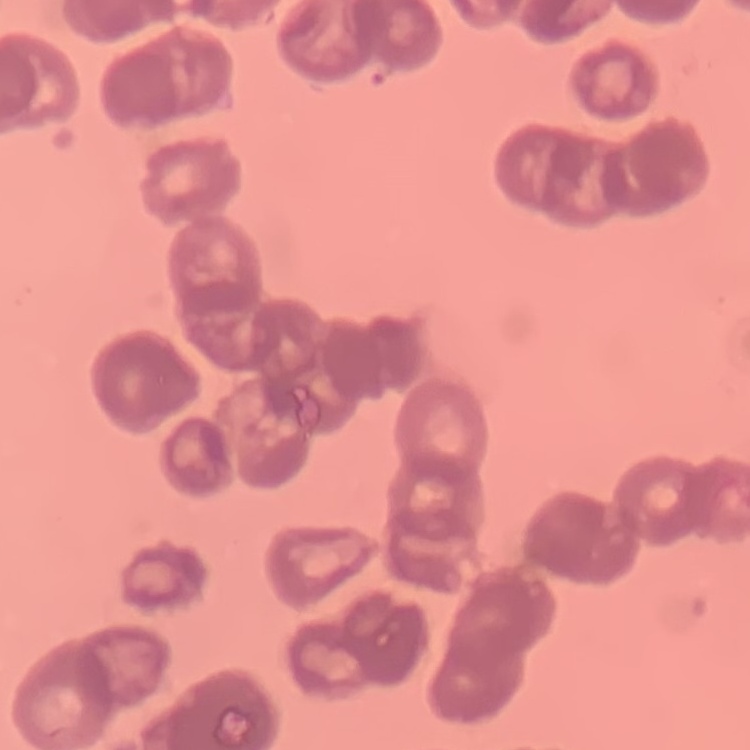
The erythrocytes show rouleaux formation. Field's or Giemsa stain. Square crop of a larger photomicrograph. Thin peripheral smear.